State which cell type is depicted.
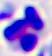
A leukocyte.

Captured at 400x magnification. Micrograph.